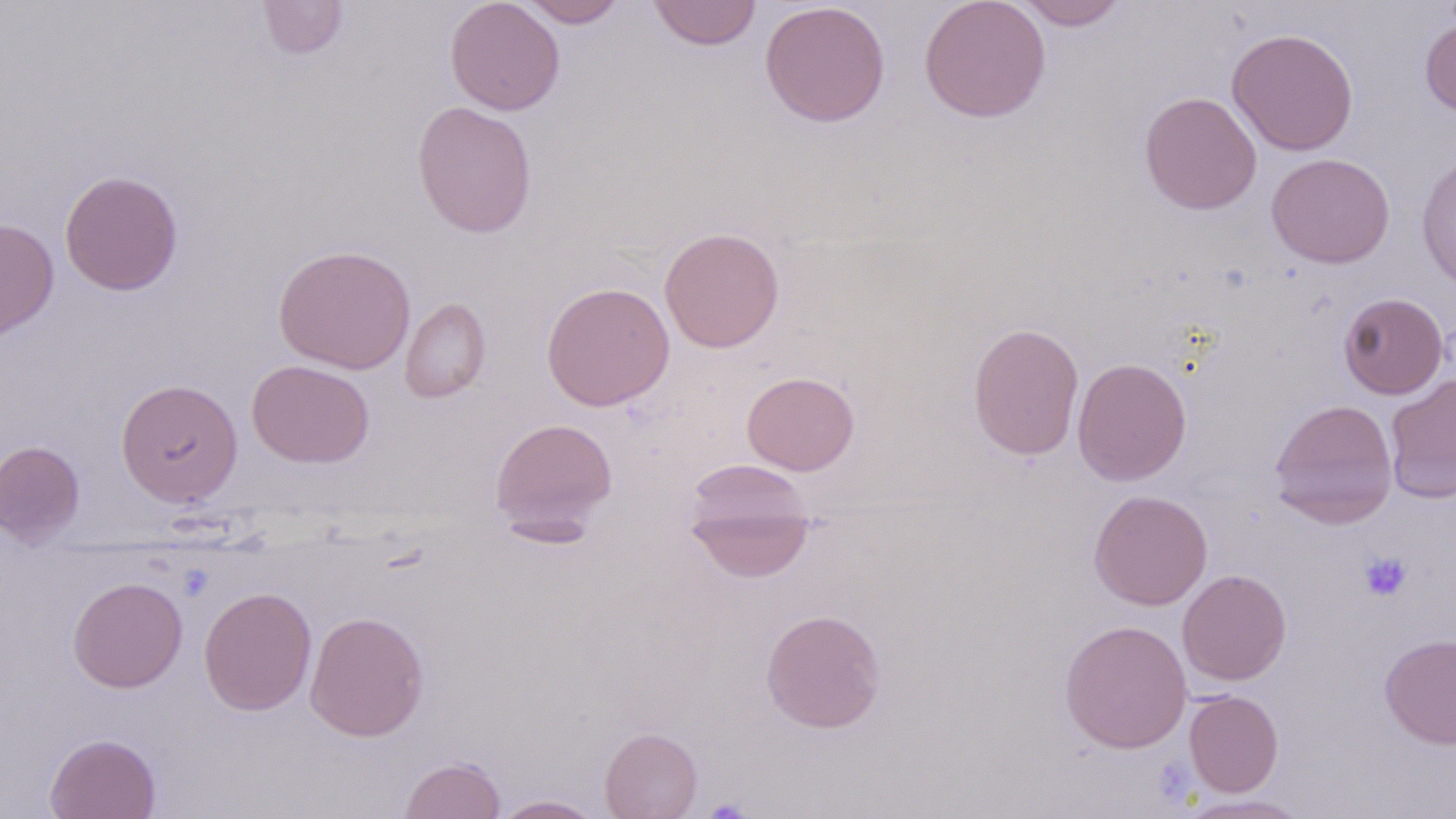 Approximate bounding boxes as named x1/y1/x2/y2 corners in pixels. Uninfected red blood cell locations: (x1=257, y1=0, x2=348, y2=59), (x1=445, y1=0, x2=565, y2=116), (x1=519, y1=0, x2=627, y2=27), (x1=648, y1=0, x2=761, y2=50), (x1=918, y1=0, x2=1051, y2=122), (x1=1015, y1=0, x2=1129, y2=30), (x1=759, y1=1, x2=890, y2=128), (x1=1420, y1=17, x2=1456, y2=117), (x1=1226, y1=27, x2=1359, y2=156), (x1=1139, y1=91, x2=1262, y2=215), (x1=411, y1=101, x2=537, y2=238), (x1=1266, y1=153, x2=1395, y2=268), (x1=1416, y1=154, x2=1456, y2=291), (x1=59, y1=169, x2=183, y2=296), (x1=0, y1=218, x2=59, y2=341), (x1=659, y1=226, x2=784, y2=353), (x1=273, y1=244, x2=416, y2=374), (x1=541, y1=281, x2=675, y2=412), (x1=1337, y1=292, x2=1450, y2=399), (x1=399, y1=297, x2=491, y2=403), (x1=967, y1=322, x2=1085, y2=461), (x1=1072, y1=357, x2=1192, y2=486), (x1=247, y1=359, x2=374, y2=468), (x1=742, y1=371, x2=860, y2=476), (x1=1384, y1=373, x2=1456, y2=504), (x1=115, y1=378, x2=243, y2=507), (x1=1269, y1=399, x2=1398, y2=528), (x1=489, y1=417, x2=618, y2=540), (x1=0, y1=440, x2=85, y2=546), (x1=683, y1=459, x2=816, y2=582), (x1=1088, y1=488, x2=1213, y2=610), (x1=1177, y1=569, x2=1292, y2=686), (x1=67, y1=576, x2=188, y2=693), (x1=199, y1=586, x2=317, y2=715), (x1=760, y1=608, x2=886, y2=733), (x1=304, y1=610, x2=428, y2=742), (x1=1059, y1=619, x2=1192, y2=753), (x1=1379, y1=632, x2=1456, y2=749), (x1=1184, y1=690, x2=1284, y2=797), (x1=600, y1=727, x2=702, y2=819), (x1=44, y1=733, x2=160, y2=819), (x1=399, y1=756, x2=506, y2=819), (x1=1174, y1=794, x2=1315, y2=818), (x1=492, y1=795, x2=605, y2=818). Platelet locations: (x1=1358, y1=551, x2=1412, y2=601), (x1=703, y1=799, x2=752, y2=818). Slide-level diagnosis: no evidence of blood parasites. Image is 1456×819 pixels. Thin blood smear. Light microscopy. 1000x magnification. May-Grünwald-Giemsa-stained preparation. Single field of view.